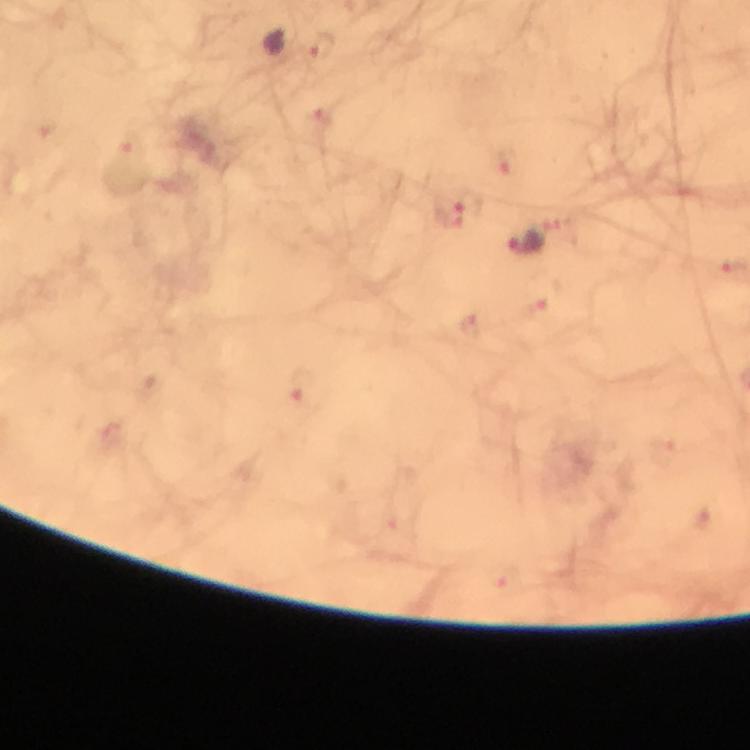
{
  "capture": "smartphone camera through the microscope",
  "context": "from a diagnostic examination for malaria",
  "preparation": "thick blood film",
  "magnification": "100x",
  "stain": "Giemsa",
  "immersion_oil": "applied",
  "image_size": "750×750 pixels",
  "cropped_from": "one field of view",
  "malaria_parasite_locations": "approximate centers as [x, y] in pixels: [321, 47], [132, 145], [508, 161], [453, 213], [524, 245], [304, 390]"
}